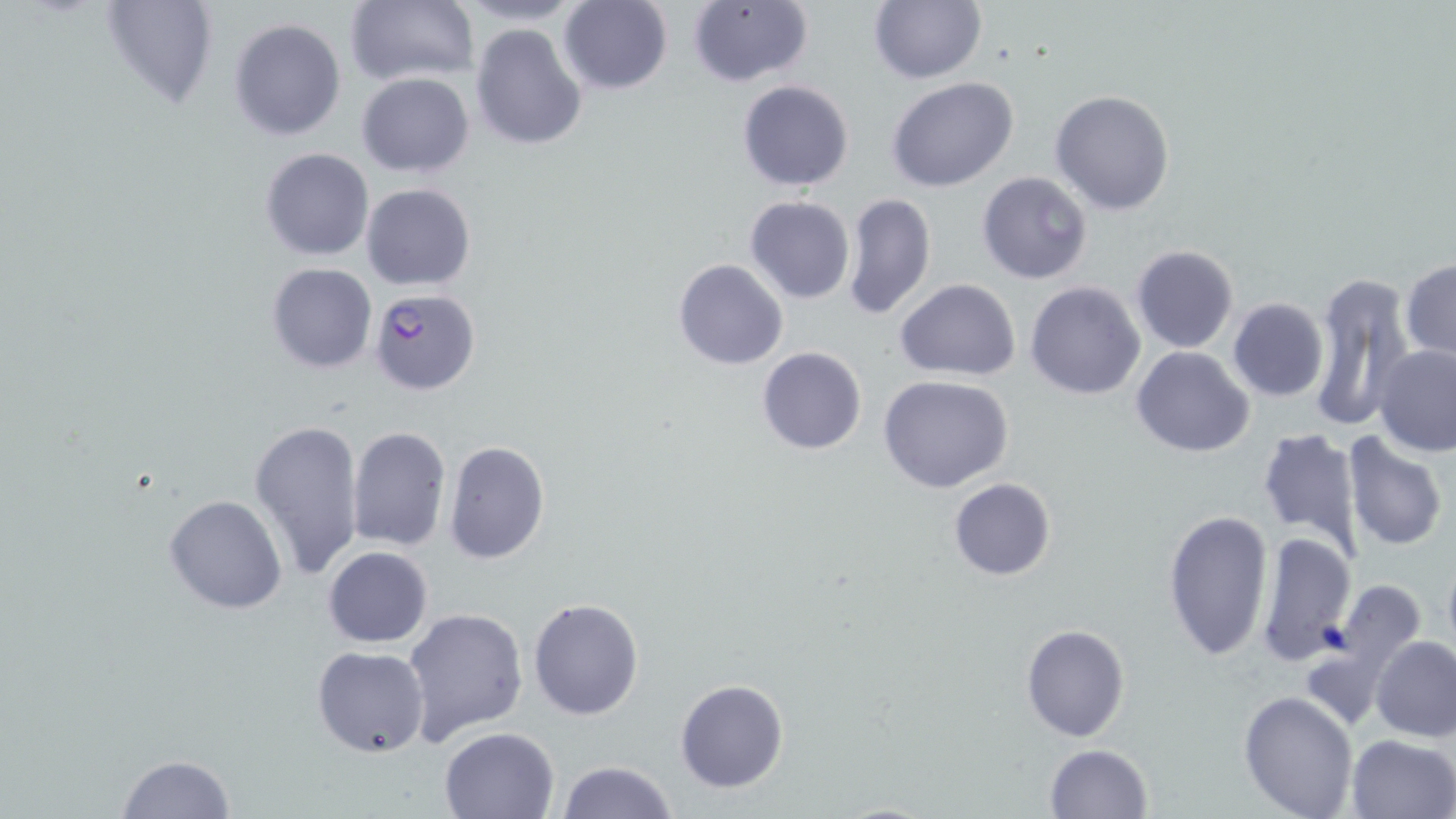 Approximate bounding boxes as named x1/y1/x2/y2 corners in pixels. Plasmodium falciparum-infected red blood cell locations: (x1=369, y1=288, x2=481, y2=395). Uninfected red blood cell locations: (x1=100, y1=0, x2=220, y2=110), (x1=345, y1=0, x2=478, y2=88), (x1=454, y1=0, x2=587, y2=26), (x1=557, y1=1, x2=673, y2=95), (x1=686, y1=1, x2=815, y2=88), (x1=867, y1=1, x2=987, y2=85), (x1=228, y1=17, x2=346, y2=140), (x1=470, y1=22, x2=589, y2=150), (x1=357, y1=72, x2=475, y2=177), (x1=888, y1=77, x2=1019, y2=190), (x1=737, y1=79, x2=854, y2=191), (x1=1049, y1=90, x2=1175, y2=215), (x1=260, y1=148, x2=375, y2=262), (x1=976, y1=171, x2=1092, y2=283), (x1=361, y1=183, x2=477, y2=291), (x1=841, y1=191, x2=936, y2=322), (x1=744, y1=196, x2=855, y2=304), (x1=1131, y1=245, x2=1239, y2=353), (x1=1401, y1=257, x2=1456, y2=362), (x1=674, y1=259, x2=787, y2=370), (x1=267, y1=262, x2=378, y2=373), (x1=1309, y1=271, x2=1414, y2=435), (x1=895, y1=278, x2=1021, y2=381), (x1=1025, y1=282, x2=1146, y2=401), (x1=1227, y1=298, x2=1328, y2=401), (x1=1372, y1=344, x2=1456, y2=456), (x1=1132, y1=345, x2=1255, y2=458), (x1=757, y1=346, x2=868, y2=455), (x1=878, y1=375, x2=1016, y2=495), (x1=249, y1=421, x2=365, y2=579), (x1=347, y1=425, x2=449, y2=551), (x1=1256, y1=426, x2=1366, y2=557), (x1=1342, y1=433, x2=1449, y2=552), (x1=444, y1=440, x2=550, y2=565), (x1=947, y1=478, x2=1056, y2=582), (x1=164, y1=493, x2=289, y2=614), (x1=1162, y1=507, x2=1273, y2=662), (x1=1254, y1=531, x2=1354, y2=668), (x1=323, y1=546, x2=433, y2=647), (x1=1441, y1=552, x2=1456, y2=661), (x1=1327, y1=576, x2=1428, y2=689), (x1=529, y1=597, x2=644, y2=720), (x1=403, y1=607, x2=529, y2=743), (x1=1019, y1=623, x2=1131, y2=743), (x1=1371, y1=635, x2=1456, y2=741), (x1=312, y1=646, x2=431, y2=757), (x1=675, y1=679, x2=789, y2=793), (x1=1239, y1=690, x2=1359, y2=818), (x1=439, y1=726, x2=559, y2=818), (x1=1347, y1=733, x2=1456, y2=818), (x1=1044, y1=744, x2=1154, y2=819), (x1=116, y1=754, x2=238, y2=818), (x1=556, y1=760, x2=678, y2=819). Slide-level diagnosis: Plasmodium falciparum. Thin blood smear. Image is 1456×819 pixels. Light microscopy. Single field of view. Captured at 1000x magnification. May-Grünwald-Giemsa stain.